Report the malaria status of this cell.
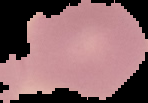
It is uninfected.

Summary:
  - Preparation: thin blood smear
  - Image type: cell region segmented out of the field of view; surrounding area masked to black
  - Image size: 148×103 pixels